Assess this cell for malaria.
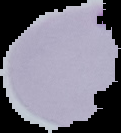
It is uninfected.

From a thin blood smear. The area outside the segmented cell region is set to black. Image is 121×133 pixels.